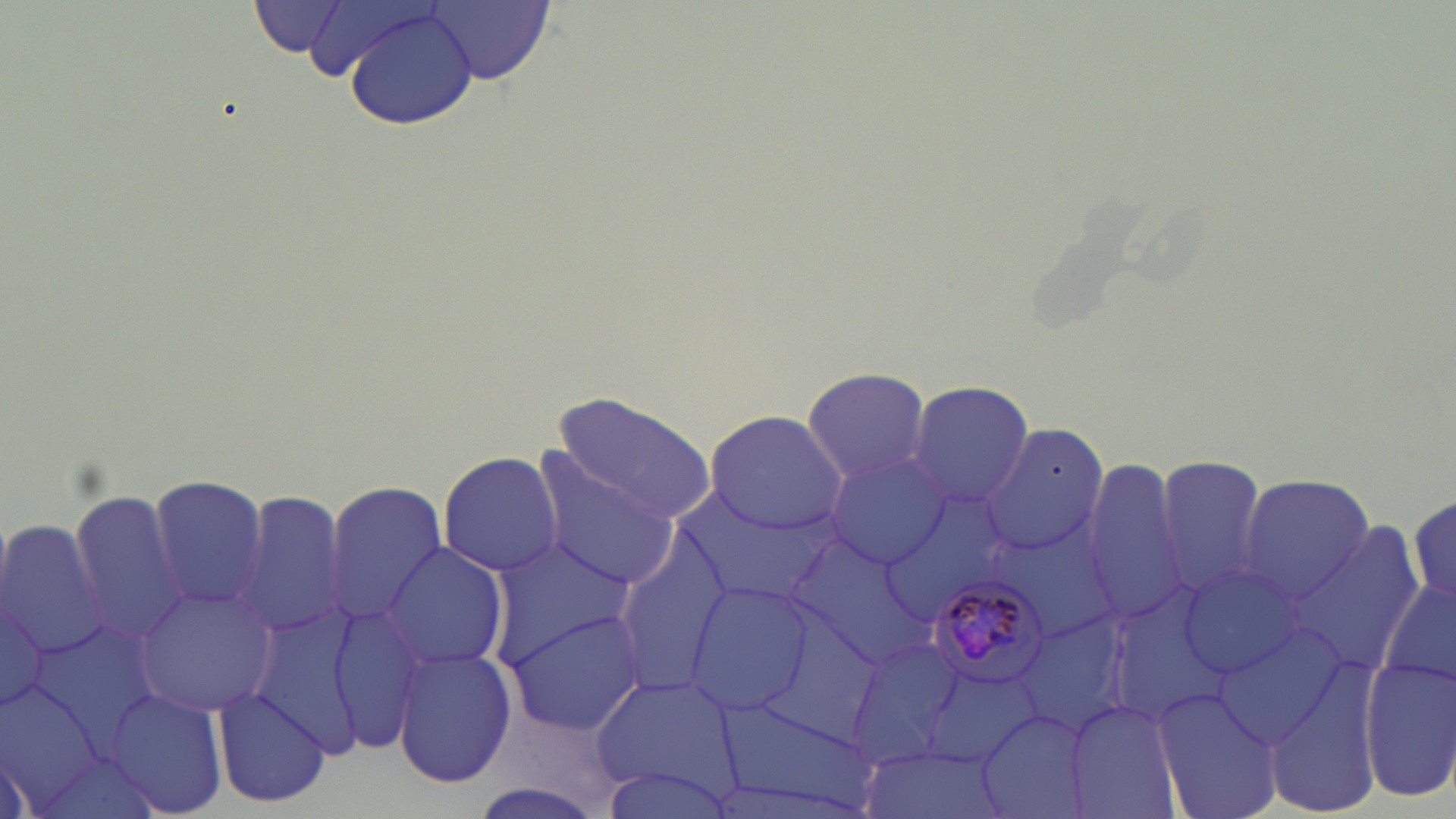
Approximate bounding boxes as (x1,y1)-(x2,y2) corner pairs in pixels. Plasmodium malariae-infected red blood cell locations: (924,578)-(1054,691). Uninfected red blood cell locations: (284,0)-(444,81), (252,1)-(351,58), (421,1)-(554,83), (343,9)-(482,130), (801,365)-(932,484), (908,380)-(1032,507), (547,393)-(720,522), (703,408)-(847,535), (984,425)-(1108,557), (530,448)-(681,592), (437,450)-(562,575), (825,452)-(952,569), (1154,453)-(1271,596), (1086,459)-(1188,619), (1236,473)-(1376,606), (145,475)-(269,611), (325,480)-(446,621), (235,487)-(351,642), (67,489)-(194,649), (1409,490)-(1454,607), (679,495)-(831,600), (0,517)-(112,665), (991,522)-(1124,646), (1287,523)-(1427,677), (615,530)-(735,700), (790,533)-(931,667), (485,540)-(635,666), (382,543)-(509,669), (1178,564)-(1308,679), (0,571)-(64,727), (1379,571)-(1456,703), (683,580)-(814,716), (135,585)-(281,715), (275,601)-(432,751), (506,608)-(649,735), (1018,613)-(1134,735), (1214,620)-(1348,750), (845,634)-(968,766), (393,647)-(517,788), (1263,656)-(1386,819), (1358,658)-(1456,800), (918,664)-(1044,766), (590,673)-(738,798), (0,680)-(112,812), (1152,685)-(1284,819), (210,686)-(331,807), (108,688)-(230,814), (1064,698)-(1182,819), (715,699)-(881,818), (976,705)-(1095,819), (857,747)-(1002,819), (596,764)-(736,819). Slide-level diagnosis: Plasmodium malariae. 1000x magnification. Light microscopy. Image is 1456×819 pixels. One field of a larger specimen. Thin blood smear. May-Grünwald-Giemsa-stained preparation.